Identify the parasite.
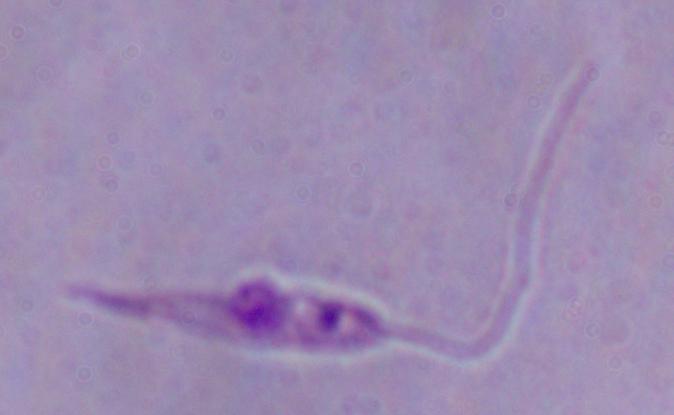

This is Leishmania.

1000x magnification. Photomicrograph.